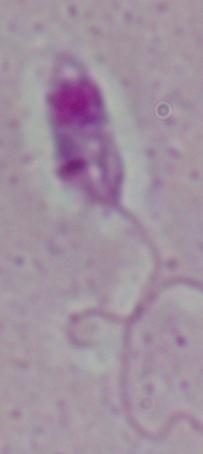

Summary:
  - Modality: micrograph
  - Identification: Leishmania
  - Magnification: 1000x